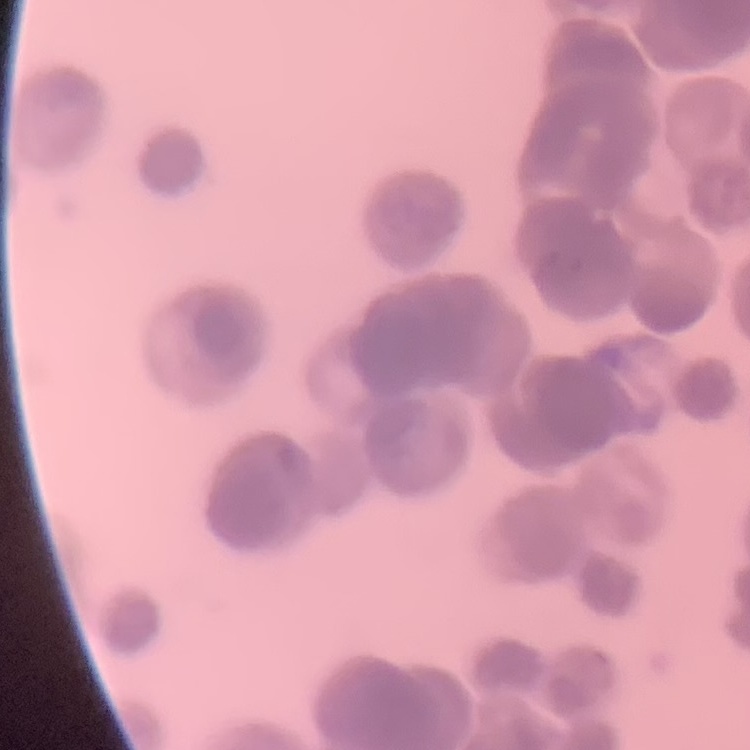

Summary:
  - Erythrocyte morphology: rouleaux formation
  - Image type: one tile cut from a larger photomicrograph
  - Preparation: thin peripheral smear
  - Stain: Field's or Giemsa